Report the malaria status of this cell.
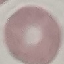

Uninfected.

Summary:
  - Stain: Giemsa
  - Image type: cell patch, automatically extracted from a larger field of view and resized to 64 × 64 pixels
  - Capture: smartphone camera at the microscope eyepiece
  - Preparation: thin blood smear